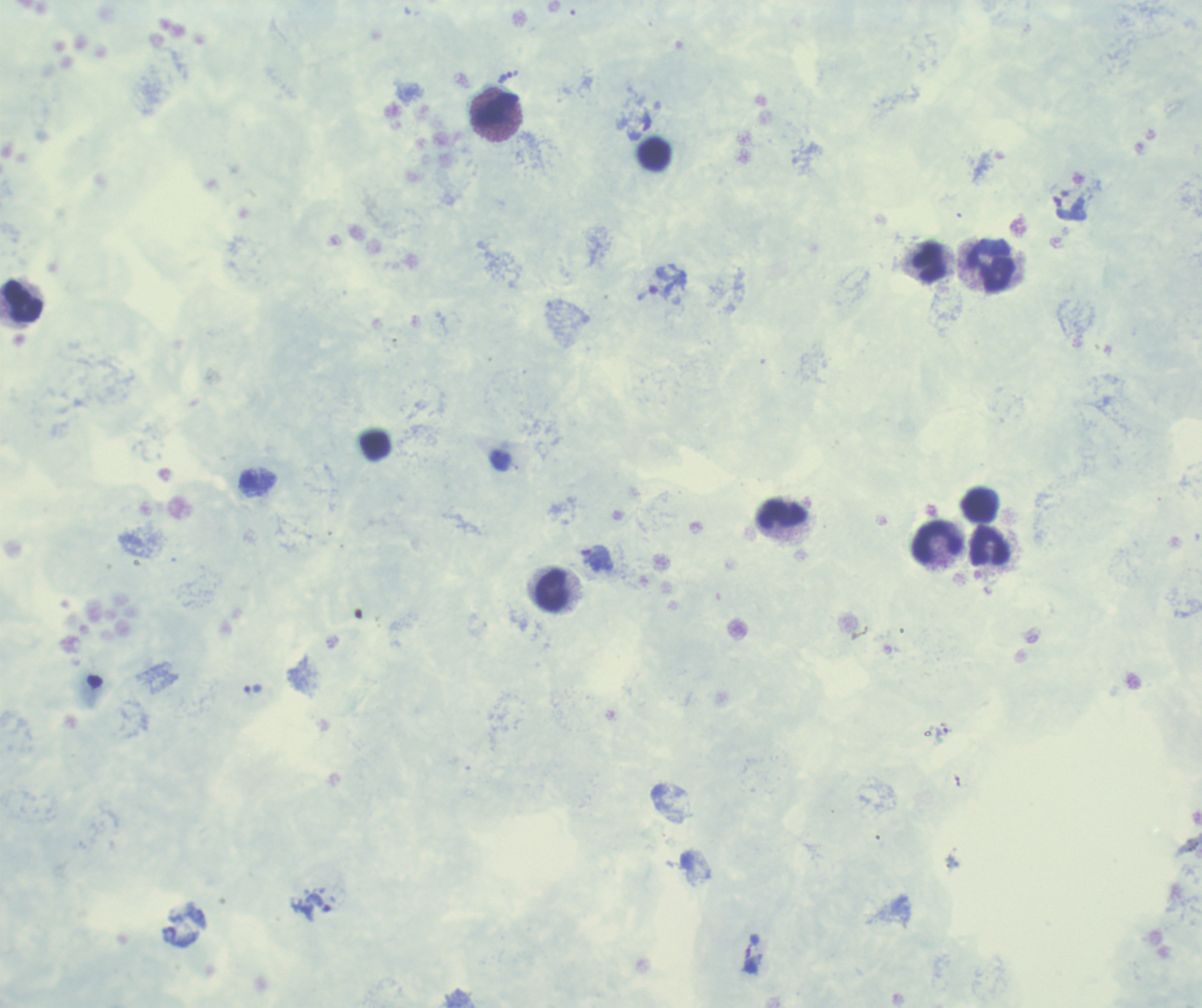 Approximate centers as (x, y) in pixels. Leukocyte locations: (497, 113), (655, 154), (931, 264), (992, 266), (21, 301), (980, 505), (783, 518), (938, 544), (990, 546), (551, 590). Trophozoite locations: (507, 77), (651, 293), (594, 558), (254, 689), (318, 904). Previously used in a real diagnosis. Thick blood film. 100x magnification. Romanowsky stain. Background quality: poor. One field from this slide. Image is 1202×1008 pixels. Result: positive for Plasmodium parasites.